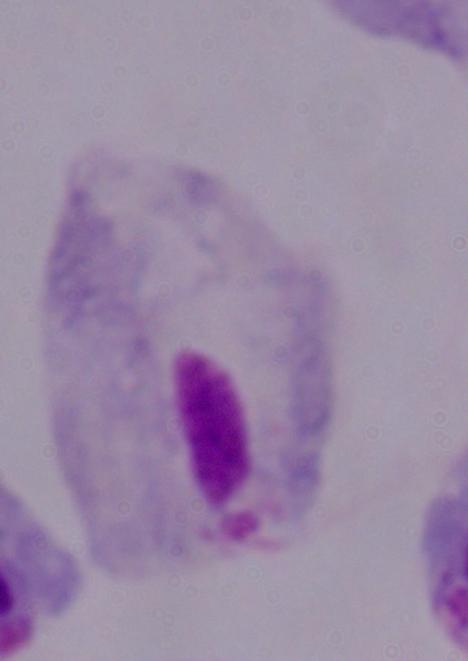
identification: trichomonad
modality: photomicrograph
magnification: 1000x